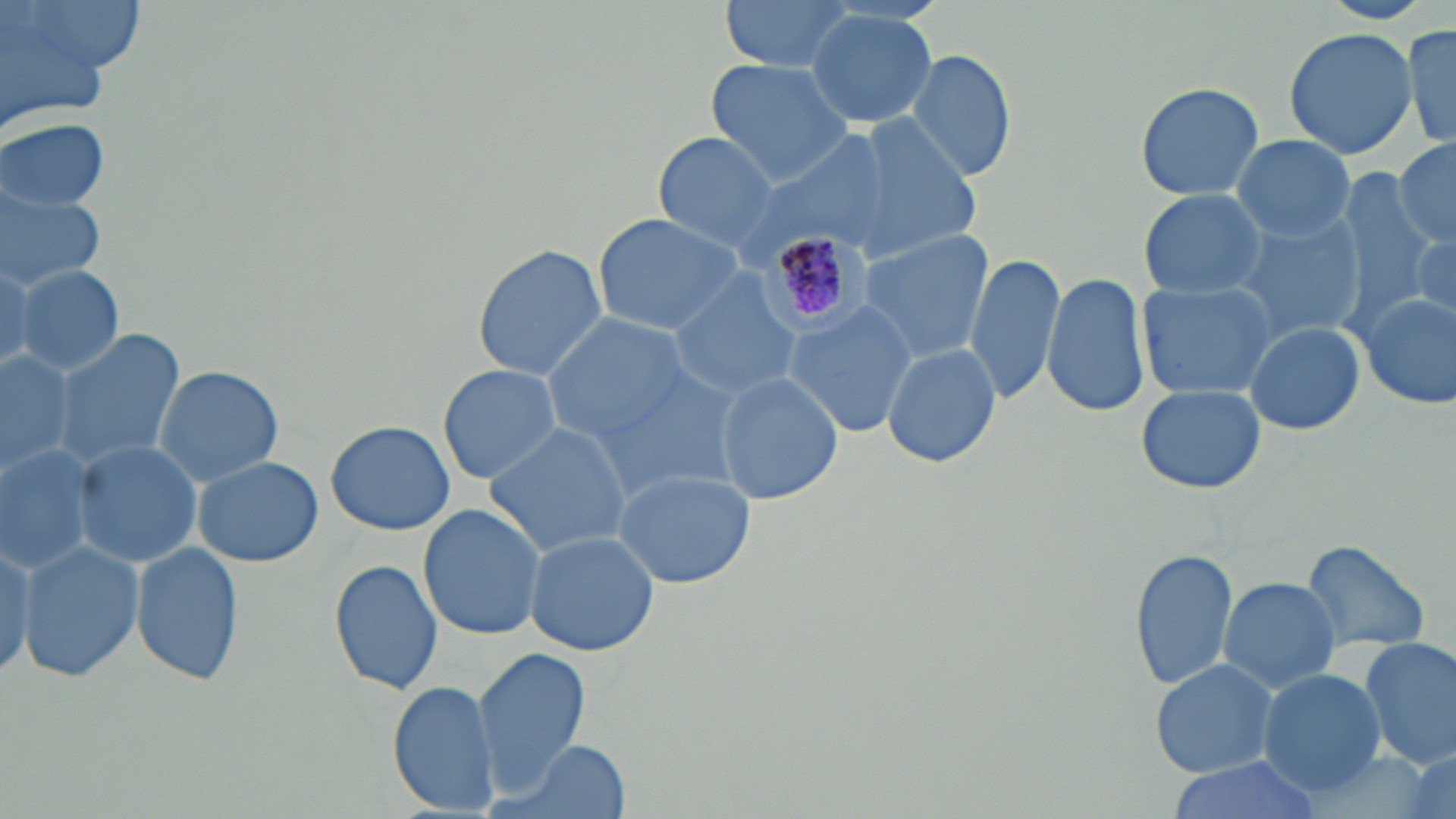
Summary:
  - Coordinate format: approximate bounding boxes as (x1,y1)-(x2,y2) corner pairs in pixels
  - Plasmodium malariae-infected red blood cell locations: (751,220)-(870,342)
  - Uninfected red blood cell locations: (16,0)-(145,78), (717,0)-(865,75), (0,1)-(126,137), (805,9)-(938,128), (1406,22)-(1456,153), (1282,26)-(1418,159), (907,48)-(1018,184), (703,58)-(857,185), (1135,79)-(1264,203), (821,113)-(985,263), (0,118)-(113,213), (651,132)-(782,254), (1232,136)-(1356,241), (739,139)-(888,258), (1393,139)-(1456,246), (0,184)-(109,290), (1138,188)-(1270,301), (590,213)-(746,336), (1228,213)-(1367,343), (1387,214)-(1456,328), (857,230)-(992,361), (1409,236)-(1454,320), (474,241)-(608,382), (966,251)-(1063,405), (0,260)-(36,373), (14,266)-(124,376), (667,268)-(802,397), (1041,270)-(1150,419), (1138,282)-(1281,400), (1356,291)-(1455,410), (783,301)-(918,435), (546,316)-(697,444), (1246,322)-(1365,435), (53,329)-(186,469), (881,343)-(1001,467), (0,349)-(77,477), (154,364)-(284,486), (438,364)-(562,484), (597,370)-(739,498), (713,373)-(843,504), (1136,384)-(1265,494), (324,420)-(455,536), (483,423)-(633,559), (72,439)-(202,568), (0,443)-(97,573), (192,456)-(323,567), (612,468)-(758,589), (418,503)-(546,639), (524,531)-(659,655), (1299,538)-(1433,653), (18,539)-(144,686), (0,540)-(33,683), (131,541)-(246,688), (1130,547)-(1238,691), (329,559)-(443,695), (1219,577)-(1343,695), (1359,638)-(1456,771), (473,645)-(591,797), (1151,659)-(1279,778), (1257,668)-(1388,795), (387,682)-(499,815), (494,739)-(629,819), (1163,758)-(1330,819)
  - Slide-level diagnosis: Plasmodium malariae
  - Field of view: single
  - Modality: light microscopy
  - Preparation: thin blood film
  - Stain: May-Grünwald-Giemsa
  - Image size: 1456×819 pixels
  - Magnification: 1000x